Comment on the morphology of the red blood cells.
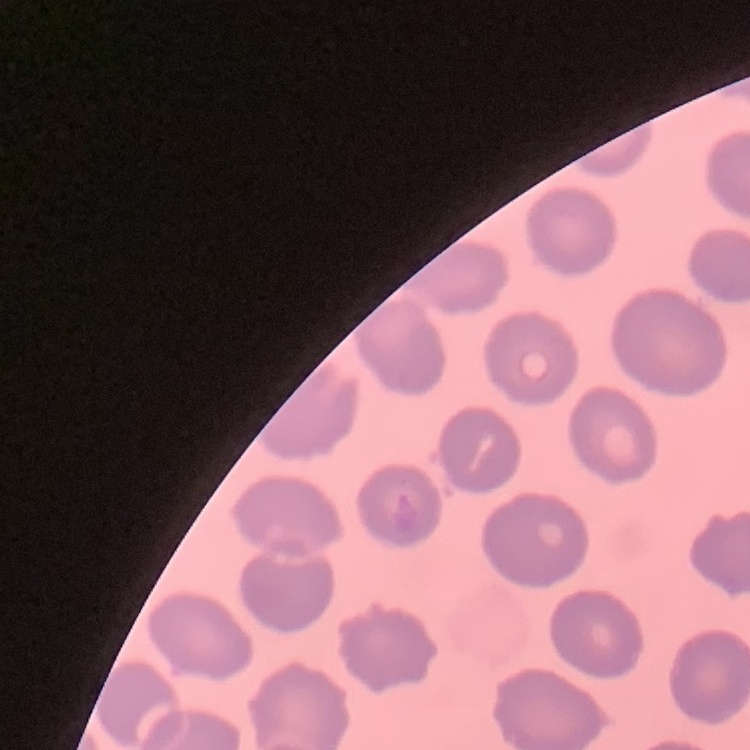

No rouleaux formation.

Summary:
  - Preparation: thin blood smear
  - Stain: Field's or Giemsa
  - Image type: one tile cut from a larger photomicrograph